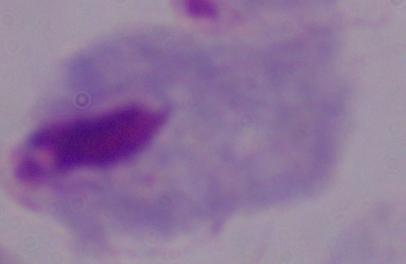

Summary:
  - Modality: micrograph
  - Identification: trichomonad
  - Magnification: 1000x